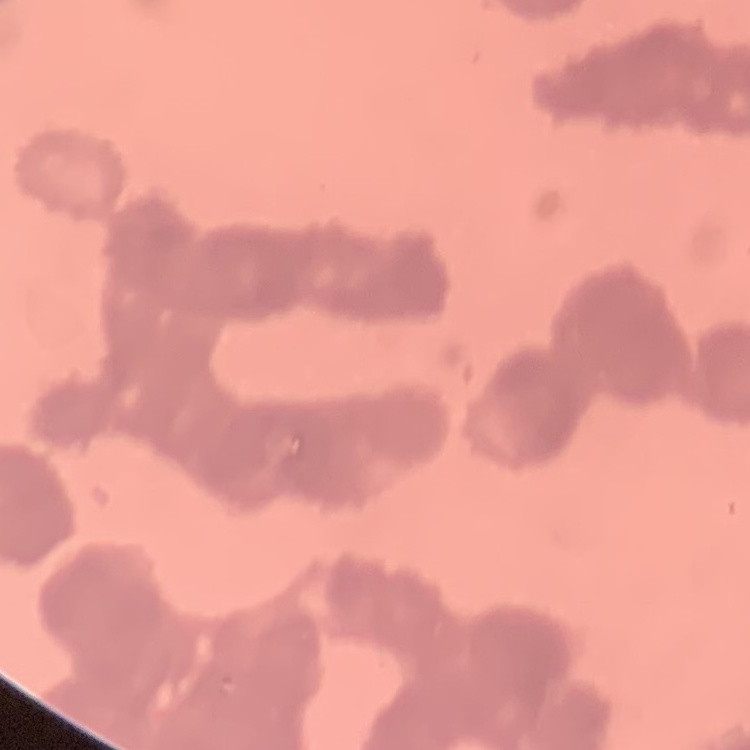 The red blood cells exhibit rouleaux formation. Thin blood smear. One tile cut from a larger photomicrograph. Stained with either Field's or Giemsa.